Assess this cell for malaria.
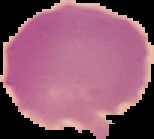
Uninfected.

Image is 154×139 pixels. Segmented cell region on a black background. From a thin blood smear.